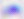

Summary:
  - Identification: Toxoplasma gondii
  - Magnification: 400x
  - Modality: photomicrograph